Identify the parasite.
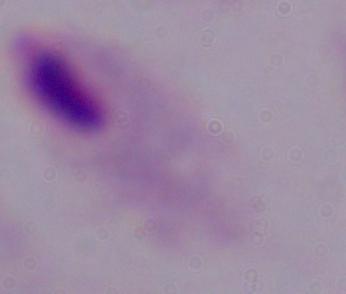
This is a trichomonad.

{
  "magnification": "1000x",
  "modality": "photomicrograph"
}